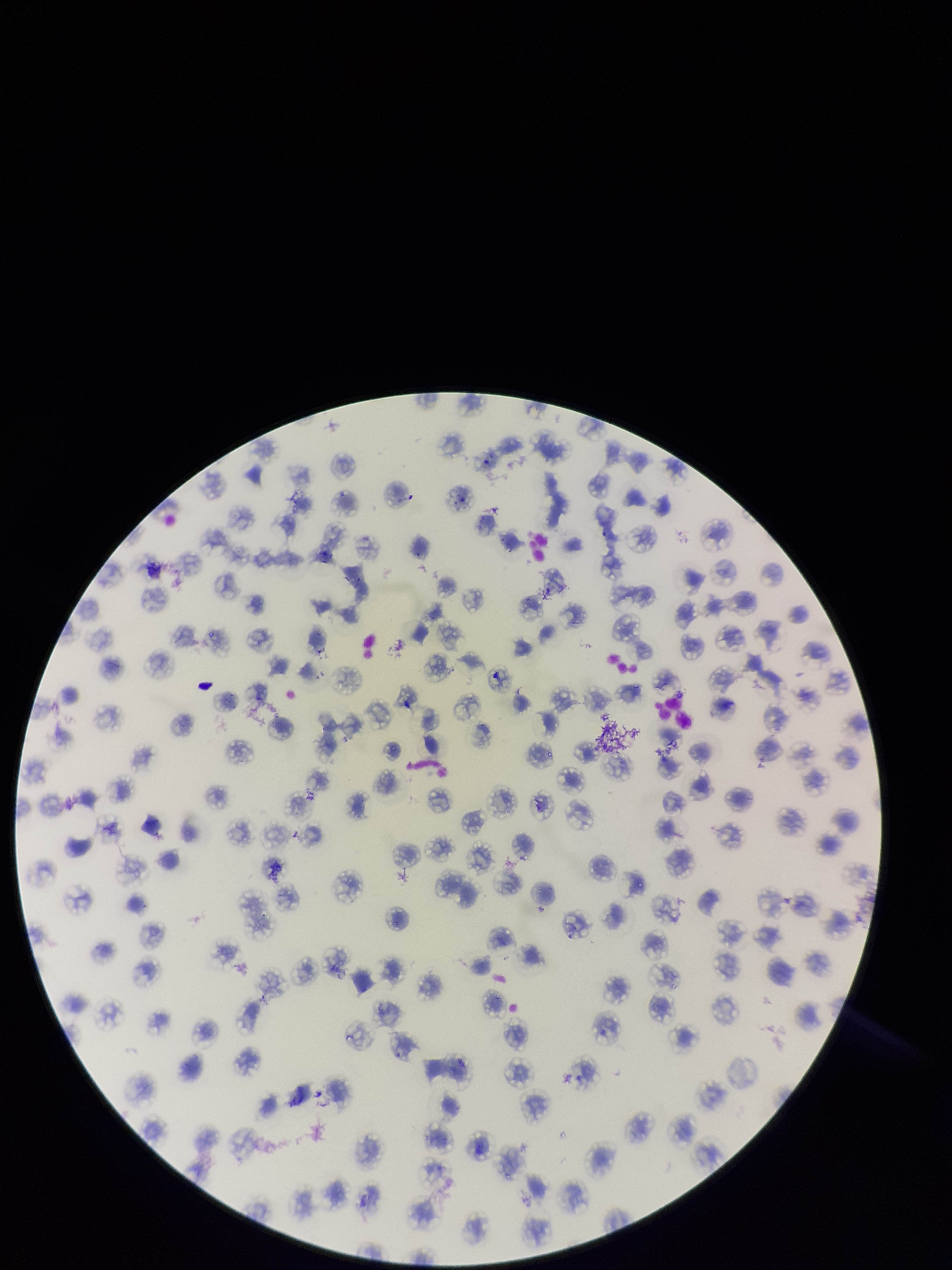
preparation: thin
species_reported_for_this_patient: Plasmodium falciparum
stain: Giemsa
patient_malaria_status: positive
red_blood_cell_count: 113
image_size: 952×1270 pixels
parasitized_red_blood_cell_count: 0
field_of_view: one from this slide
capture: smartphone photograph through the microscope eyepiece
parasitized_red_blood_cells: none detected